Assess this cell for malaria.
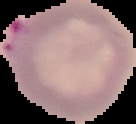
It is parasitized.

Segmented cell region on a black background. Image is 136×124 pixels. From a thin blood film.